State which parasite is depicted.
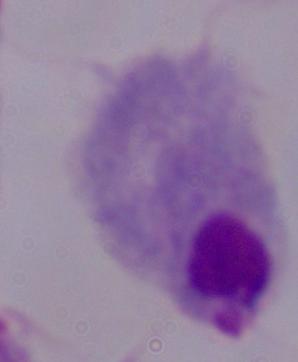
A trichomonad.

magnification = 1000x
modality = photomicrograph